Classify this cell by malaria status.
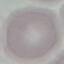

It is uninfected.

Summary:
  - Capture: smartphone through the microscope eyepiece
  - Image type: cell patch, automatically extracted from a larger field of view and resized to 64 × 64 pixels
  - Preparation: thin smear
  - Stain: Giemsa